Give the position of every leukocyte visible.
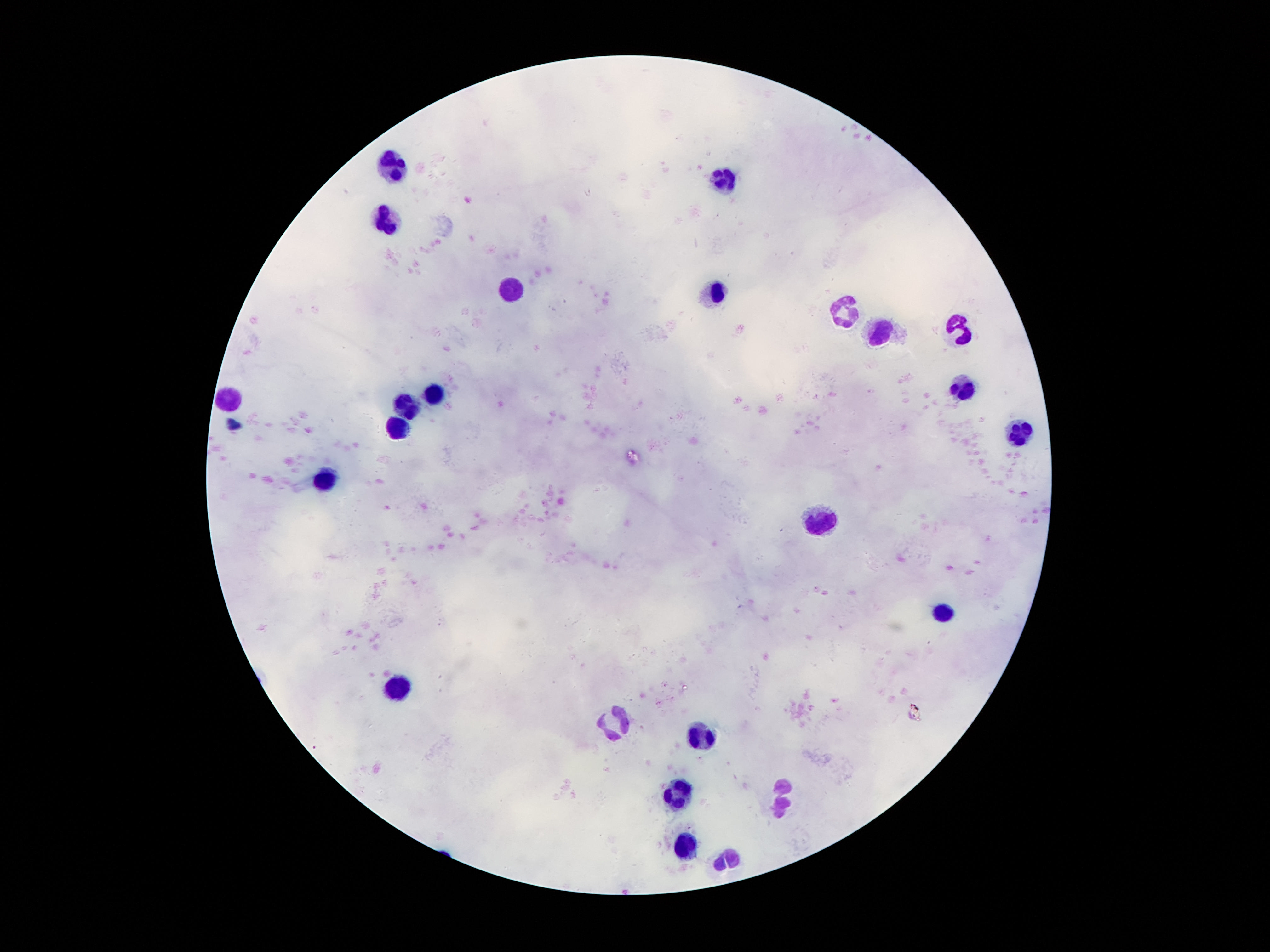
Approximate centers as [x, y] in pixels.
Leukocytes: [390, 164], [726, 177], [386, 221], [512, 288], [711, 292], [848, 311], [959, 328], [879, 332], [961, 389], [432, 393], [230, 397], [409, 402], [394, 427], [1018, 437], [323, 477], [820, 517], [942, 609], [398, 688], [617, 724], [701, 736], [673, 789], [785, 799], [686, 845], [726, 861].

Summary:
  - Preparation: thick blood film
  - Magnification: 100x
  - Stain: Giemsa
  - Patient malaria status: uninfected
  - Field of view: one from this slide
  - Image size: 1270×952 pixels
  - Capture: smartphone camera through the microscope eyepiece